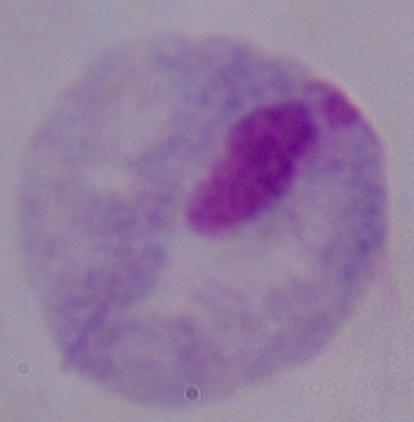

magnification = 1000x
modality = photomicrograph
identification = trichomonad